Outline each Plasmodium ovale-infected red blood cell.
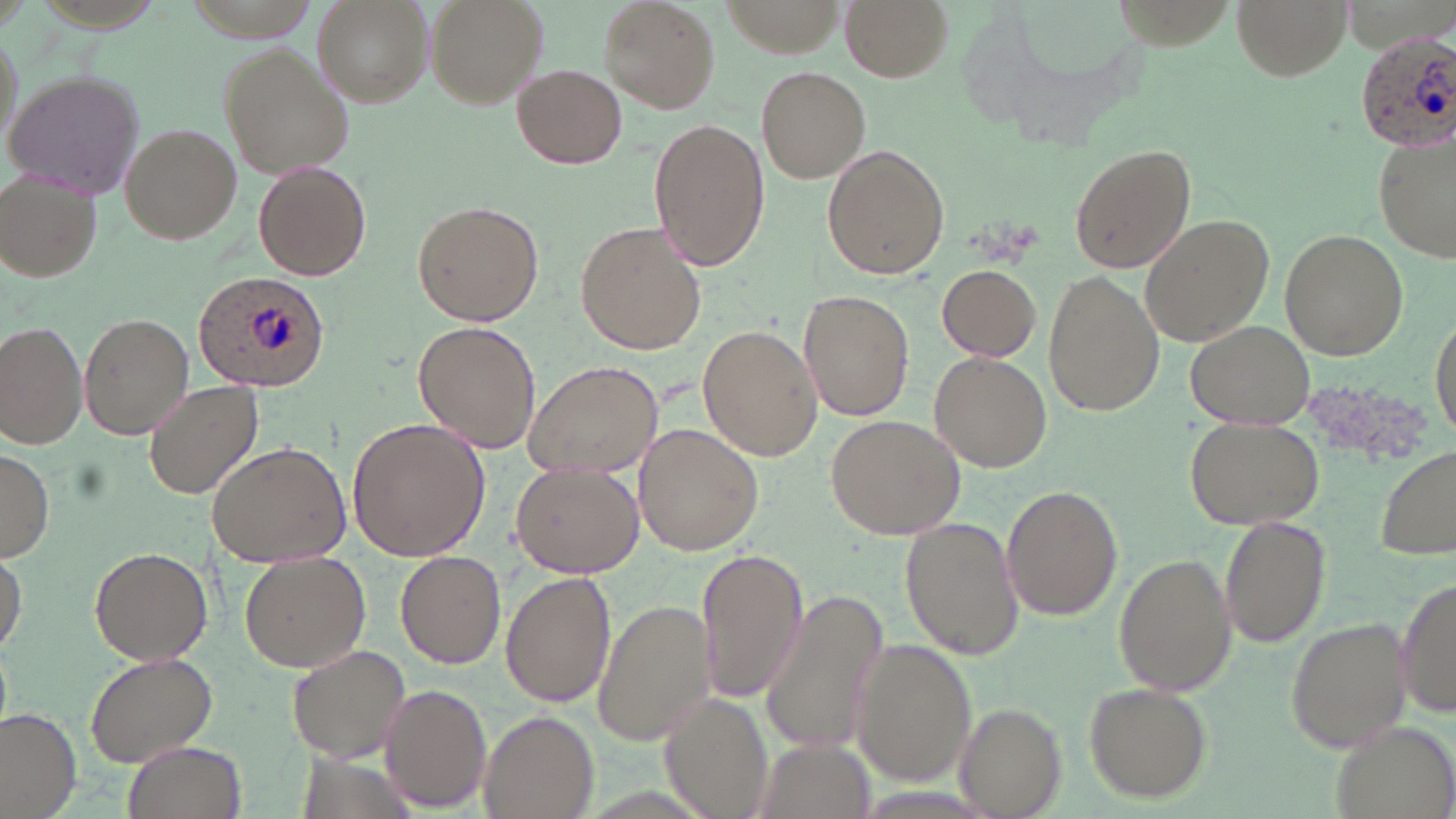

Approximate bounding boxes as [x1, y1, x2, y2] in pixels.
Plasmodium ovale-infected red blood cells: [1355, 28, 1456, 150], [195, 269, 331, 393].

Uninfected red blood cell locations: [422, 0, 549, 110], [599, 0, 720, 113], [842, 0, 952, 82], [1230, 0, 1351, 81], [312, 1, 428, 107], [219, 45, 352, 177], [512, 65, 627, 169], [757, 67, 869, 182], [4, 70, 148, 198], [649, 118, 769, 271], [120, 123, 241, 244], [1375, 129, 1453, 266], [1068, 141, 1197, 275], [822, 145, 950, 282], [254, 161, 372, 280], [3, 174, 104, 280], [414, 201, 545, 326], [1140, 212, 1275, 347], [578, 220, 711, 354], [1279, 228, 1408, 359], [938, 264, 1043, 360], [1043, 270, 1164, 415], [800, 289, 915, 422], [79, 311, 194, 438], [1430, 313, 1456, 442], [1184, 319, 1315, 429], [413, 321, 542, 453], [1, 322, 87, 449], [697, 327, 821, 460], [931, 351, 1052, 472], [523, 357, 664, 479], [146, 380, 264, 499], [827, 414, 964, 539], [1185, 416, 1324, 529], [345, 418, 491, 560], [636, 424, 766, 554], [208, 441, 354, 568], [1377, 444, 1455, 559], [0, 448, 54, 561], [510, 463, 644, 578], [1000, 486, 1124, 620], [900, 516, 1024, 660], [1218, 516, 1332, 649], [88, 545, 214, 664], [0, 546, 26, 655], [697, 548, 809, 699], [395, 552, 507, 668], [1113, 553, 1237, 696], [239, 554, 371, 673], [1395, 571, 1455, 723], [500, 572, 616, 707], [758, 590, 893, 757], [592, 597, 715, 745], [1285, 614, 1414, 755], [850, 638, 977, 785], [286, 644, 412, 762], [85, 649, 222, 768], [1083, 680, 1213, 803], [378, 683, 491, 811], [661, 692, 774, 819], [954, 703, 1066, 817], [0, 707, 82, 816], [480, 710, 599, 819], [1327, 718, 1456, 819], [749, 738, 877, 819], [121, 740, 246, 819]. Slide-level diagnosis: Plasmodium ovale. Single field of view. Captured at 1000x magnification. May-Grünwald-Giemsa-stained preparation. Thin blood smear. Light microscopy. Image is 1456×819 pixels.